Assess the morphology of the erythrocytes.
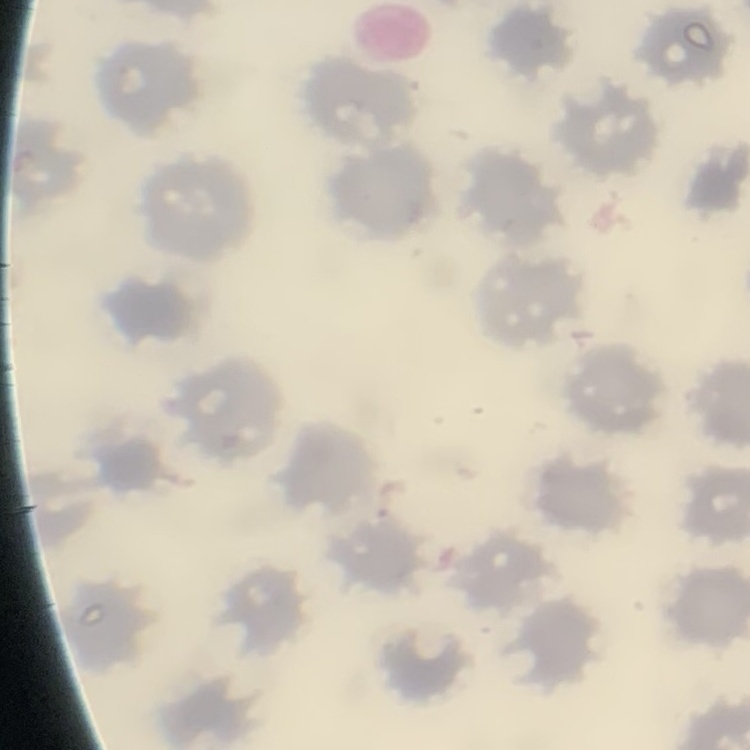
No rouleaux formation.

One tile cut from a larger photomicrograph. Stained with either Field's or Giemsa. Thin blood film.